Classify this cell by malaria status.
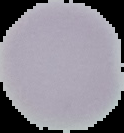
Uninfected.

image_size: 124×133 pixels
image_type: segmented cell region on a black background
preparation: thin blood film